Report the malaria status of this cell.
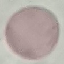

Uninfected.

Summary:
  - Image type: automatically extracted cell patch, resized to 64 × 64 pixels
  - Preparation: thin smear
  - Stain: Giemsa
  - Capture: smartphone through the microscope eyepiece